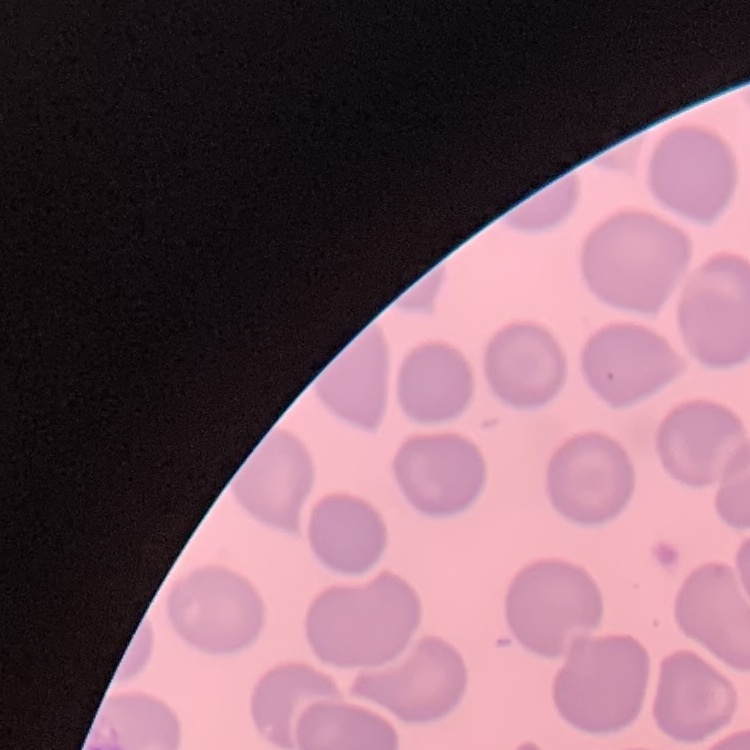
red_blood_cell_morphology: no rouleaux formation
preparation: thin peripheral smear
image_type: square crop of a larger photomicrograph
stain: Field's or Giemsa